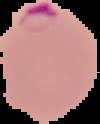
Summary:
  - Preparation: thin blood film
  - Image size: 100×124 pixels
  - Result: Plasmodium parasites detected
  - Image type: cell region segmented out of the field of view; surrounding area masked to black